Locate every blood parasite and identify its species.
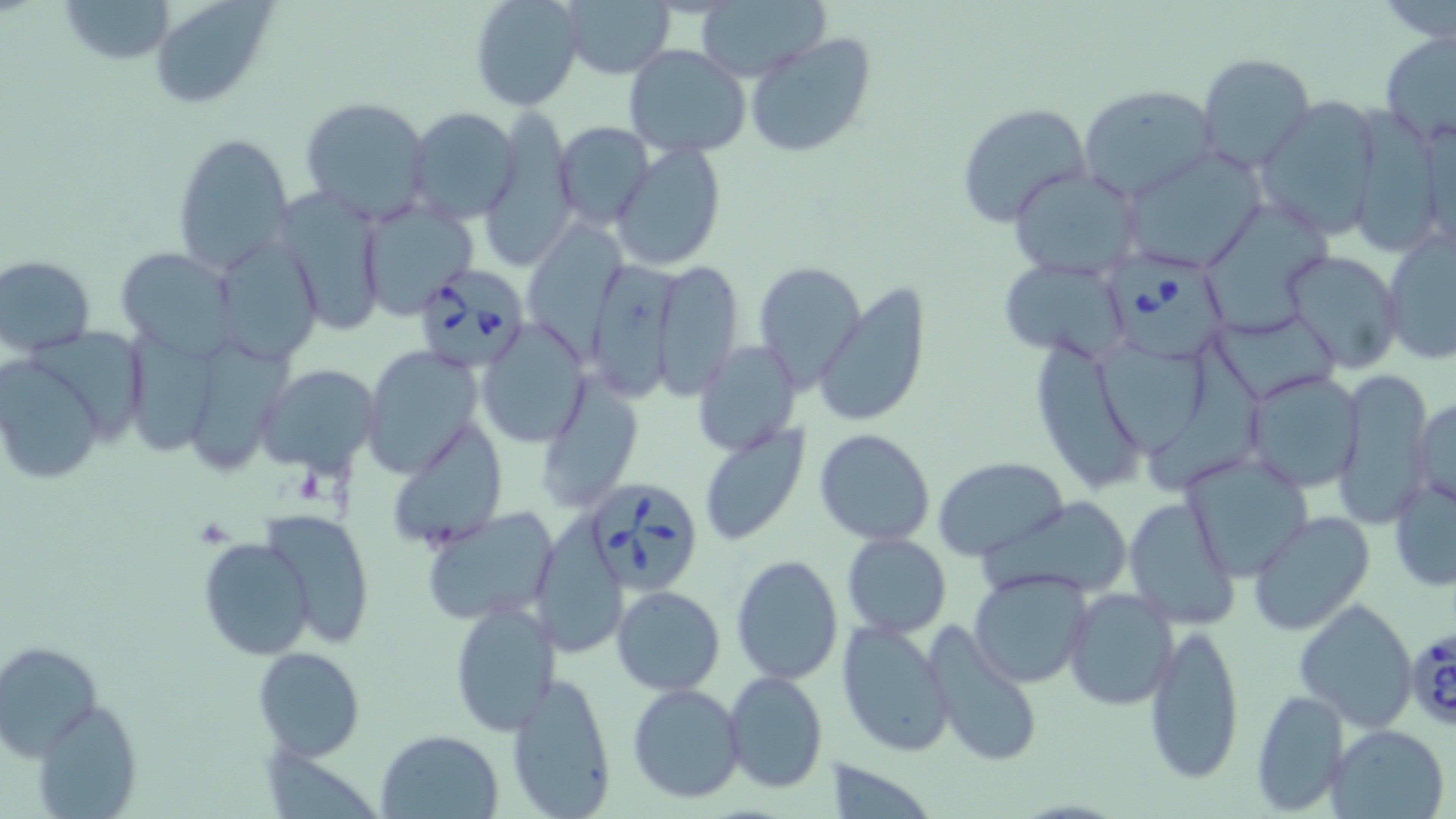

Approximate bounding boxes as [x1, y1, x2, y2] in pixels.
Babesia divergens-infected red blood cells: [1106, 250, 1234, 366], [410, 264, 534, 375], [582, 475, 705, 600], [1406, 626, 1456, 731].
No Plasmodium falciparum, Plasmodium ovale, Plasmodium malariae, Plasmodium vivax, or Trypanosoma brucei observed.

Uninfected red blood cell locations: [59, 0, 176, 65], [148, 0, 274, 108], [470, 0, 586, 111], [556, 0, 676, 79], [693, 1, 830, 82], [744, 31, 878, 159], [1379, 33, 1456, 148], [623, 45, 752, 157], [1197, 53, 1317, 175], [1079, 85, 1219, 201], [1254, 95, 1385, 241], [300, 97, 433, 225], [956, 102, 1094, 228], [406, 106, 523, 225], [478, 112, 582, 268], [552, 122, 653, 230], [171, 133, 295, 273], [610, 140, 727, 271], [1121, 152, 1264, 272], [1009, 166, 1142, 280], [275, 189, 386, 339], [358, 198, 478, 320], [1201, 204, 1334, 329], [523, 219, 628, 353], [1382, 228, 1456, 365], [212, 235, 323, 363], [118, 247, 238, 359], [1280, 249, 1405, 374], [583, 254, 683, 405], [0, 255, 96, 355], [999, 258, 1132, 365], [653, 259, 743, 397], [753, 260, 864, 387], [812, 282, 932, 429], [1215, 313, 1338, 396], [477, 320, 592, 449], [25, 323, 149, 441], [126, 333, 218, 457], [1031, 337, 1143, 490], [193, 339, 298, 470], [695, 340, 802, 456], [1094, 340, 1211, 454], [1149, 341, 1271, 488], [361, 346, 484, 479], [0, 355, 108, 485], [255, 363, 379, 472], [1333, 367, 1430, 525], [1243, 370, 1365, 494], [536, 376, 643, 514], [1410, 398, 1453, 506], [387, 420, 507, 551], [698, 422, 811, 549], [813, 429, 937, 546], [1180, 450, 1315, 581], [935, 457, 1067, 561], [1388, 472, 1456, 593], [988, 496, 1135, 602], [1122, 497, 1239, 632], [421, 506, 562, 627], [259, 508, 376, 649], [1247, 511, 1376, 636], [541, 513, 627, 657], [841, 532, 952, 639], [198, 536, 313, 660], [731, 554, 844, 686], [969, 570, 1092, 690], [611, 584, 725, 695], [1063, 588, 1179, 712], [1294, 598, 1419, 732], [448, 600, 560, 736], [837, 618, 958, 759], [1142, 620, 1245, 784], [926, 624, 1044, 771], [0, 640, 102, 759], [254, 647, 365, 759], [724, 669, 828, 794], [505, 670, 617, 818], [627, 683, 745, 804], [1250, 689, 1349, 815], [32, 697, 142, 818], [1326, 725, 1450, 818], [379, 729, 506, 818]. Slide-level diagnosis: Babesia divergens. Thin blood film. Image is 1456×819 pixels. Captured at 1000x magnification. One field of a larger specimen. Optical microscopy. May-Grünwald-Giemsa-stained preparation.